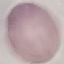
Malaria status: uninfected. Thin smear of blood. Acquired by smartphone through the microscope eyepiece. Giemsa-stained preparation. Cell patch, automatically extracted from a larger field of view and resized to 64 × 64 pixels.